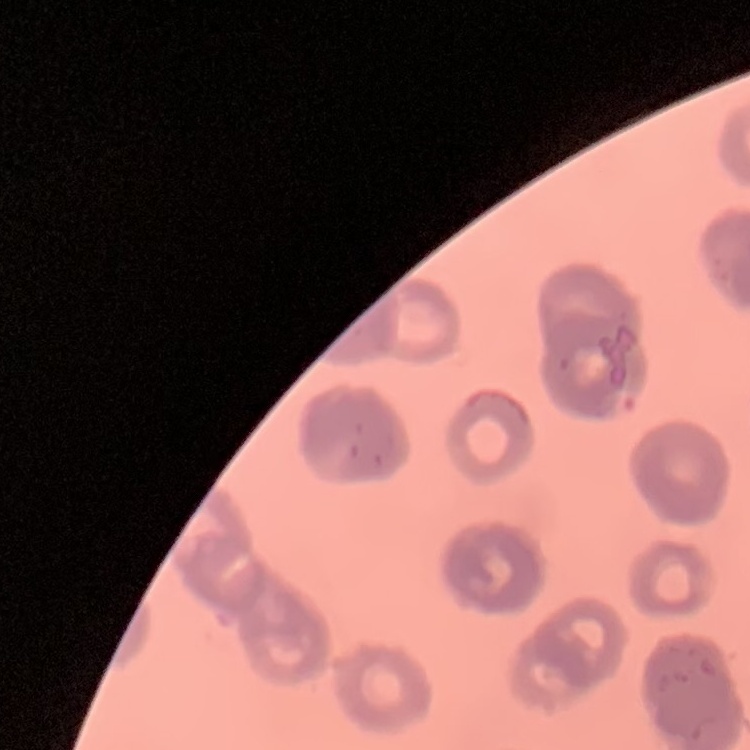 The red blood cells exhibit rouleaux formation. Square crop of a larger photomicrograph. Thin peripheral smear. Stained with either Field's or Giemsa.